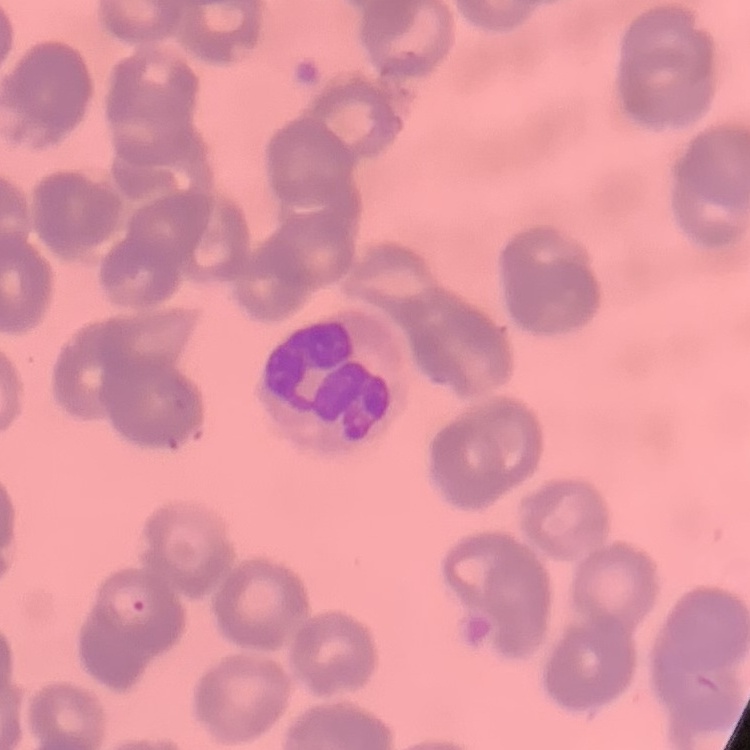

The erythrocytes show rouleaux formation. Thin peripheral smear. One tile cut from a larger photomicrograph. Stained with either Field's or Giemsa.